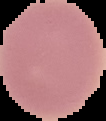 Result: negative for Plasmodium parasites. From a thin blood film. Cell region segmented out of the field of view; the surrounding area is masked to black. Image is 106×121 pixels.